Give the extent of all Plasmodium vivax-infected red blood cells.
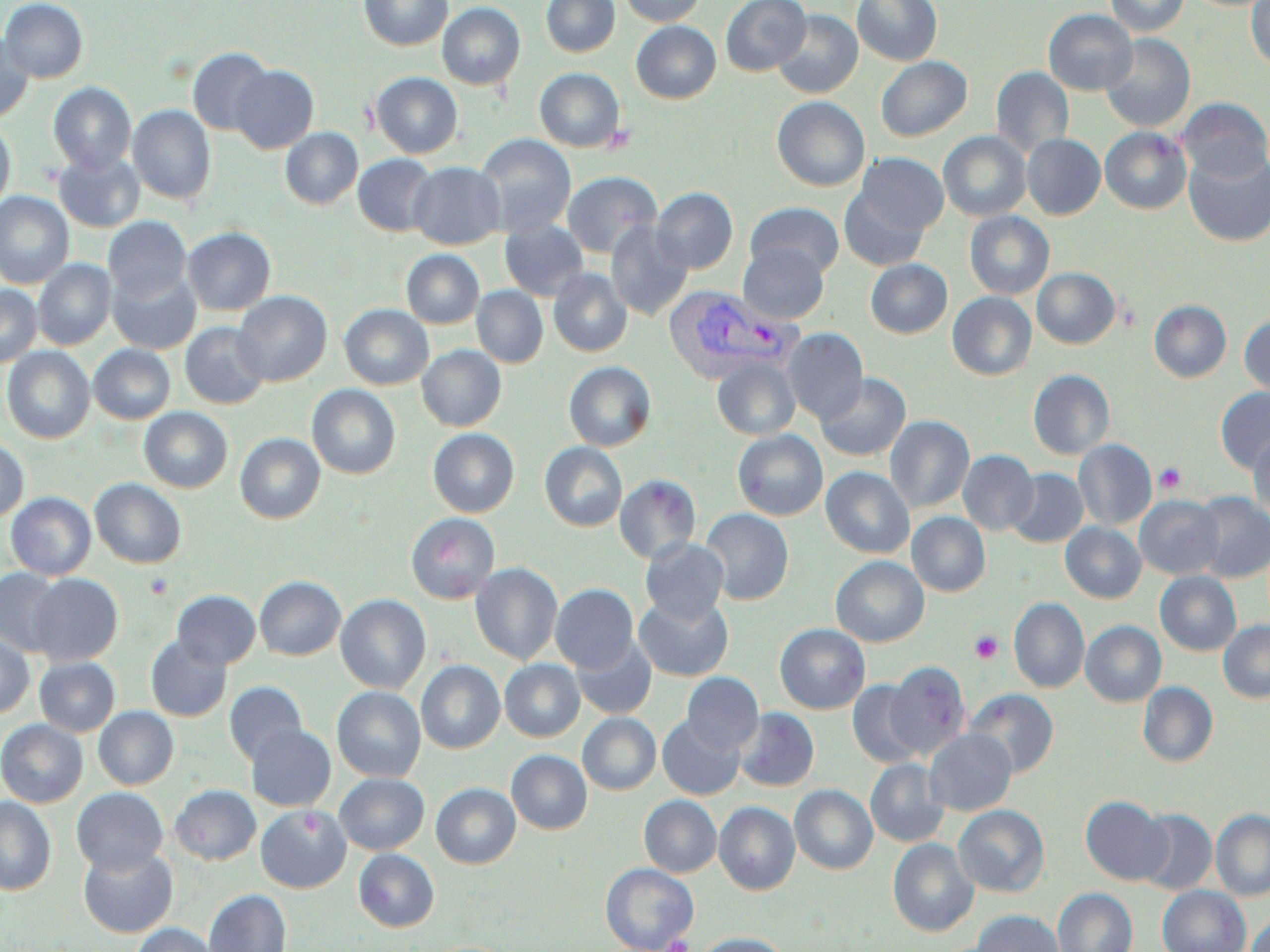

Approximate bounding boxes as (x1, y1, x2, y2) in pixels.
Plasmodium vivax-infected red blood cells: (663, 284, 800, 386).

slide_level_diagnosis: Plasmodium vivax
image_size: 1270×952 pixels
uninfected_red_blood_cell_locations: 'approximate bounding boxes as (x1, y1, x2, y2) in pixels: (0, 0, 88, 83), (358, 0, 453, 50), (541, 0, 620, 56), (619, 0, 705, 26), (720, 0, 811, 76), (853, 0, 942, 66), (1104, 0, 1190, 37), (1246, 0, 1270, 71), (437, 2, 525, 90), (772, 9, 862, 98), (1043, 9, 1137, 95), (631, 21, 721, 103), (0, 33, 35, 122), (1100, 34, 1195, 132), (187, 47, 274, 135), (876, 56, 972, 141), (230, 65, 319, 153), (990, 66, 1074, 157), (535, 68, 625, 152), (370, 72, 463, 158), (48, 82, 136, 174), (772, 96, 870, 191), (1177, 97, 1270, 183), (128, 105, 216, 204), (0, 120, 15, 212), (281, 127, 362, 209), (1100, 127, 1191, 214), (938, 131, 1030, 221), (475, 133, 576, 236), (1022, 134, 1105, 219), (53, 150, 145, 232), (1183, 150, 1270, 247), (856, 153, 949, 236), (353, 154, 439, 236), (408, 161, 505, 249), (562, 171, 662, 258), (651, 187, 738, 274), (840, 187, 930, 271), (0, 192, 73, 288), (745, 201, 845, 279), (964, 211, 1054, 299), (103, 215, 192, 303), (606, 219, 693, 321), (499, 220, 589, 300), (183, 227, 276, 315), (738, 243, 829, 323), (401, 249, 484, 328), (33, 259, 115, 349), (865, 259, 952, 338), (108, 266, 200, 353), (548, 268, 632, 356), (1032, 268, 1120, 349), (0, 285, 41, 367), (472, 286, 548, 367), (233, 291, 332, 386), (947, 291, 1036, 380), (1149, 300, 1231, 382), (339, 304, 433, 390), (1239, 314, 1270, 397), (179, 322, 270, 409), (782, 327, 868, 424), (88, 344, 175, 424), (417, 345, 506, 430), (2, 346, 95, 443), (711, 355, 801, 440), (564, 361, 656, 451), (1028, 369, 1115, 459), (816, 372, 910, 461), (307, 384, 400, 479), (1215, 387, 1270, 473), (139, 407, 232, 493), (885, 415, 974, 512), (427, 428, 519, 517), (733, 429, 828, 520), (1248, 432, 1270, 521), (235, 433, 325, 523), (0, 437, 29, 522), (1074, 439, 1156, 530), (539, 442, 627, 531), (958, 450, 1039, 535), (821, 467, 914, 558), (1006, 467, 1088, 547), (615, 474, 701, 564), (90, 478, 187, 568), (5, 492, 97, 580), (1190, 492, 1270, 583), (1135, 495, 1224, 579), (700, 508, 794, 605), (907, 512, 990, 596), (405, 513, 500, 604), (1060, 522, 1146, 603), (640, 538, 729, 624), (831, 556, 929, 646), (471, 562, 562, 665), (0, 567, 66, 656), (1155, 571, 1241, 656), (29, 573, 123, 665), (255, 575, 346, 660), (550, 583, 638, 672), (172, 590, 260, 669), (335, 594, 431, 694), (634, 595, 733, 681), (1008, 597, 1089, 693), (1079, 620, 1166, 706), (1218, 620, 1270, 703), (774, 623, 870, 714), (0, 633, 34, 718), (570, 635, 656, 719), (145, 636, 232, 722), (34, 657, 119, 736), (500, 659, 585, 741), (416, 660, 505, 753), (884, 661, 970, 758), (682, 672, 764, 753), (224, 680, 307, 765), (847, 680, 926, 768), (1137, 681, 1218, 767), (332, 686, 425, 782), (965, 689, 1059, 778), (93, 706, 178, 789), (734, 708, 819, 791), (578, 713, 661, 794), (657, 714, 744, 800), (0, 719, 88, 807), (245, 723, 336, 810), (925, 728, 1016, 816), (506, 750, 592, 834), (865, 758, 949, 847), (334, 773, 429, 854), (431, 783, 520, 868), (169, 784, 261, 865), (790, 785, 877, 874), (71, 787, 168, 874), (639, 795, 721, 877), (0, 796, 56, 895), (1080, 796, 1172, 885), (714, 801, 799, 895), (256, 804, 351, 892), (953, 804, 1049, 896), (1135, 809, 1217, 895), (1210, 809, 1270, 900), (888, 838, 978, 937), (78, 846, 178, 937), (353, 848, 439, 931), (600, 863, 699, 951), (1157, 885, 1250, 952), (1053, 888, 1137, 952), (204, 889, 291, 952), (973, 910, 1065, 952), (1247, 911, 1270, 952), (129, 923, 219, 952), (693, 933, 792, 952)'
platelet_locations: 'approximate bounding boxes as (x1, y1, x2, y2) in pixels: (600, 124, 638, 154), (1154, 463, 1186, 493), (144, 573, 174, 599), (969, 630, 1004, 663), (664, 935, 692, 952)'
preparation: thin blood smear
field_of_view: one of a larger specimen
magnification: 1000x
stain: May-Grünwald-Giemsa
modality: optical microscopy